Identify the parasite.
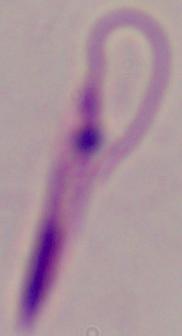
This is Leishmania.

Summary:
  - Magnification: 1000x
  - Modality: micrograph